Report the malaria status of this cell.
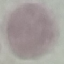
It is uninfected.

image type = automatically extracted cell patch, resized to 64 × 64 pixels
capture = smartphone through the microscope eyepiece
preparation = thin smear
stain = Giemsa